Report the malaria status of this cell.
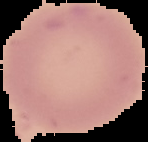

Uninfected.

image type = segmented cell region on a black background
preparation = thin blood film
image size = 148×142 pixels